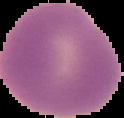

result = no malaria parasites detected
image size = 124×118 pixels
preparation = thin blood film
image type = segmented cell region with the area outside set to black